Classify this cell by malaria status.
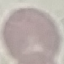
Uninfected.

preparation: thin smear
capture: smartphone through the microscope eyepiece
image_type: cell patch, automatically extracted from a larger field of view and resized to 64 × 64 pixels
stain: Giemsa